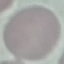

Summary:
  - Result: negative for malaria parasites
  - Image type: cell patch, automatically extracted from a larger field of view and resized to 64 × 64 pixels
  - Preparation: thin blood smear
  - Stain: Giemsa
  - Capture: smartphone through the microscope eyepiece